Name the blood parasite species.
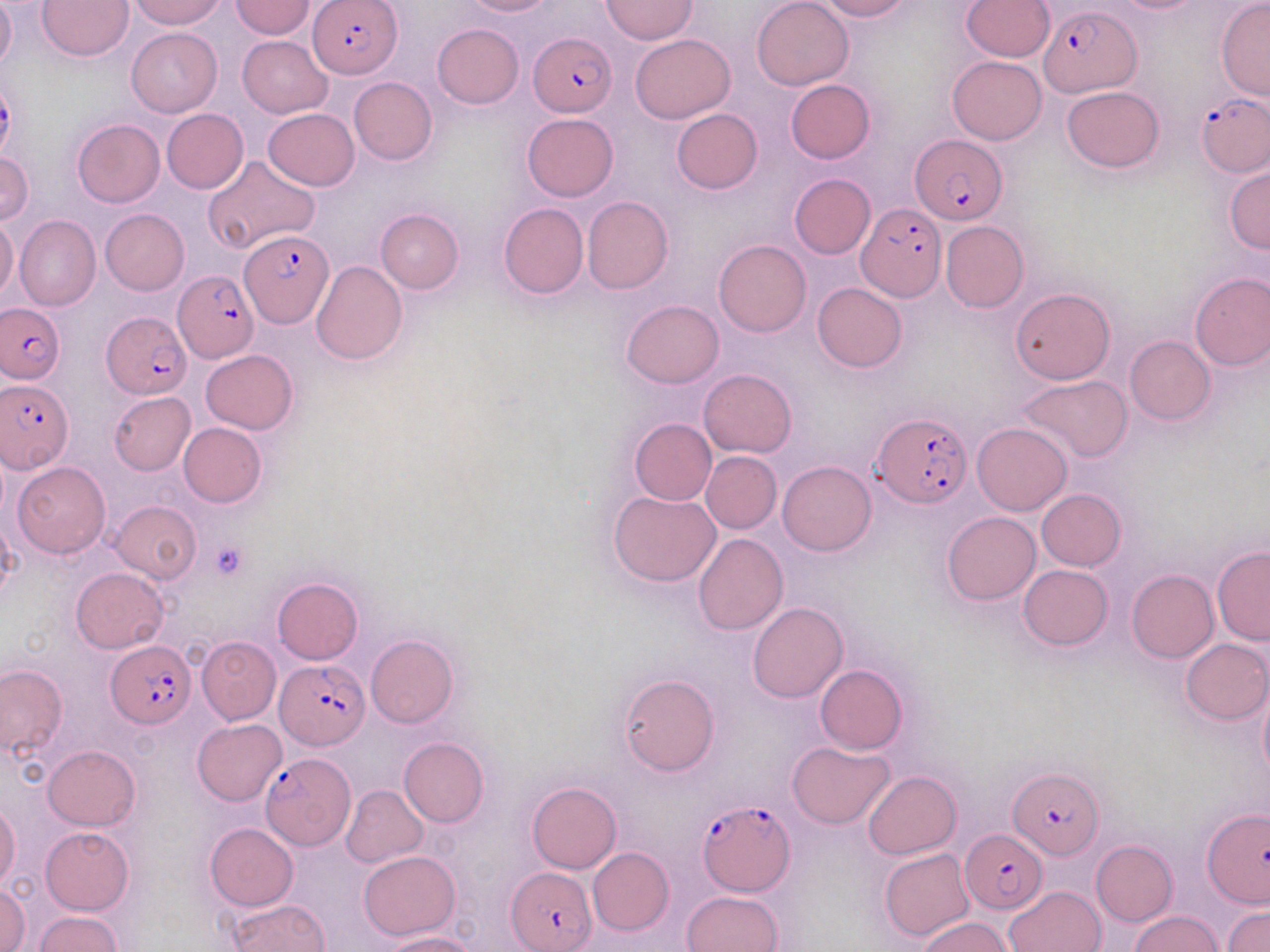
Plasmodium falciparum.

Summary:
  - Coordinate format: approximate bounding boxes as (x1,y1)-(x2,y2) corner pairs in pixels
  - Platelet locations: (209,542)-(248,579)
  - Uninfected red blood cell locations: (0,0)-(16,71), (38,0)-(132,60), (128,0)-(226,28), (461,0)-(556,16), (600,0)-(697,44), (751,0)-(854,89), (816,0)-(912,21), (961,0)-(1054,61), (1107,0)-(1207,14), (229,1)-(316,39), (1216,2)-(1270,101), (432,23)-(523,109), (127,27)-(222,118), (631,34)-(735,123), (237,35)-(332,118), (947,55)-(1046,145), (348,77)-(437,165), (785,79)-(875,164), (1061,85)-(1164,173), (263,108)-(359,191), (161,109)-(249,194), (671,109)-(762,194), (522,113)-(618,200), (73,119)-(165,208), (0,151)-(33,224), (204,156)-(320,252), (1224,166)-(1269,253), (788,174)-(876,259), (581,196)-(673,294), (498,203)-(588,298), (375,208)-(463,293), (100,209)-(189,295), (13,214)-(101,311), (0,218)-(18,300), (941,221)-(1029,312), (714,239)-(811,337), (309,261)-(407,365), (1190,272)-(1270,370), (813,282)-(907,373), (1010,287)-(1114,384), (621,299)-(725,388), (1124,335)-(1215,425), (201,349)-(298,434), (698,369)-(796,457), (1017,375)-(1133,463), (110,392)-(196,475), (629,418)-(716,505), (179,423)-(267,508), (973,423)-(1072,515), (700,451)-(781,534), (777,459)-(876,556), (11,461)-(109,559), (609,489)-(721,588), (1037,490)-(1126,571), (110,500)-(202,584), (943,512)-(1040,605), (693,532)-(787,635), (1212,547)-(1270,645), (1018,564)-(1112,650), (71,568)-(169,653), (1127,569)-(1218,662), (272,577)-(363,664), (748,602)-(847,703), (365,634)-(459,727), (197,637)-(281,724), (1181,639)-(1270,724), (0,664)-(67,756), (815,664)-(907,754), (619,674)-(718,776), (1257,682)-(1270,782), (192,719)-(287,805), (399,738)-(489,827), (787,741)-(895,829), (42,744)-(140,831), (864,770)-(961,860), (527,782)-(621,874), (341,784)-(428,867), (0,803)-(20,890), (204,823)-(297,911), (39,826)-(134,915), (1090,840)-(1178,926), (879,847)-(975,941), (588,848)-(673,935), (359,849)-(459,940), (0,882)-(30,952), (1005,885)-(1106,952), (681,890)-(784,952), (227,899)-(330,951), (1224,906)-(1270,952), (34,911)-(121,952), (1129,911)-(1221,952), (918,915)-(1015,951), (379,931)-(476,952)
  - Plasmodium falciparum-infected red blood cell locations: (309,0)-(402,78), (1040,5)-(1141,97), (528,31)-(618,119), (1197,94)-(1269,176), (910,135)-(1005,224), (858,202)-(947,303), (241,230)-(333,329), (176,267)-(261,362), (2,302)-(65,383), (103,313)-(190,399), (2,380)-(73,471), (872,411)-(971,509), (107,640)-(196,727), (276,660)-(370,751), (261,753)-(355,851), (1011,767)-(1103,857), (697,798)-(795,896), (1202,807)-(1269,908), (959,831)-(1047,915), (506,866)-(597,951)
  - Stain: May-Grünwald-Giemsa
  - Magnification: 1000x
  - Field of view: single
  - Image size: 1270×952 pixels
  - Preparation: thin blood film
  - Modality: light microscopy